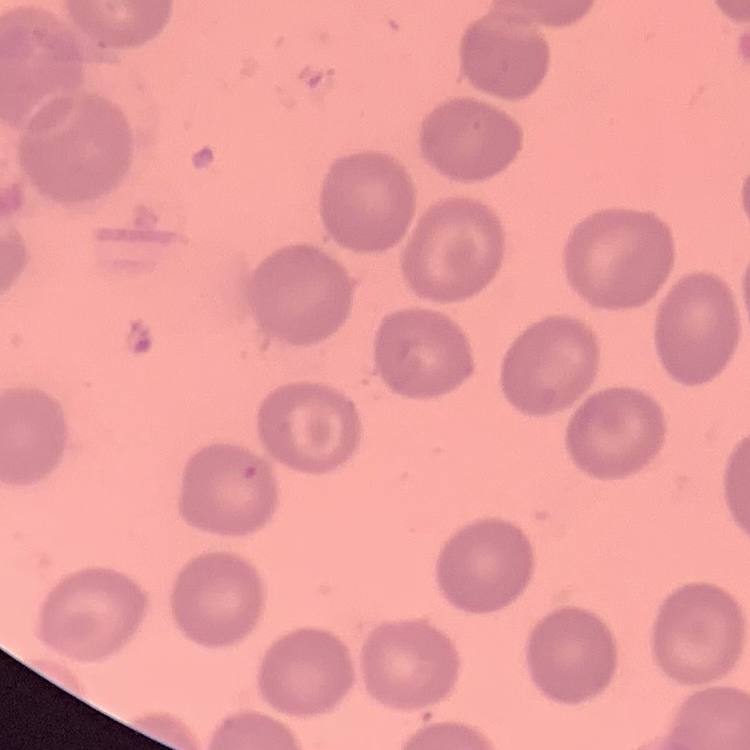
Summary:
  - Erythrocyte morphology: no rouleaux formation
  - Preparation: thin blood film
  - Image type: square crop of a larger photomicrograph
  - Stain: Field's or Giemsa